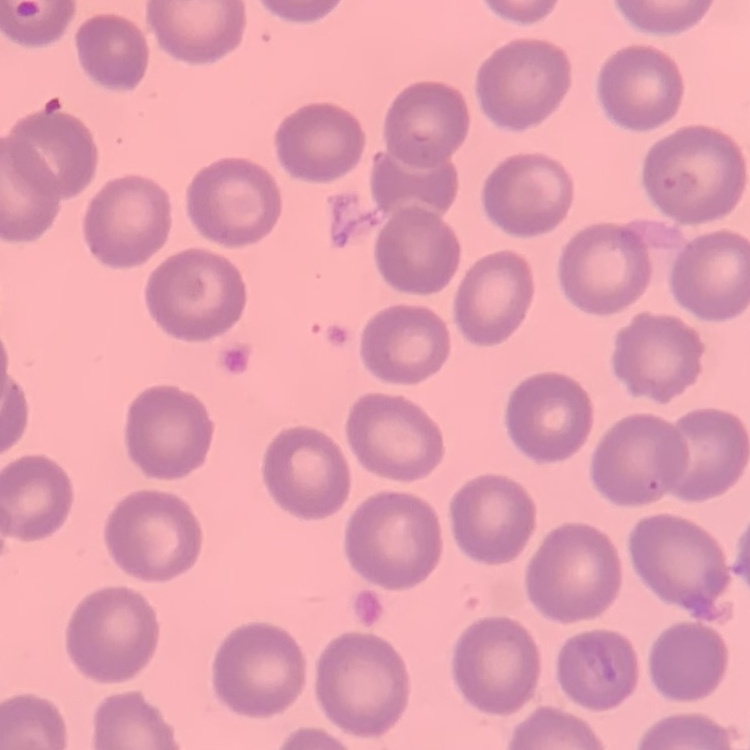

erythrocyte_morphology: no rouleaux formation
image_type: one tile cut from a larger photomicrograph
stain: Field's or Giemsa
preparation: thin blood smear